Report the malaria status.
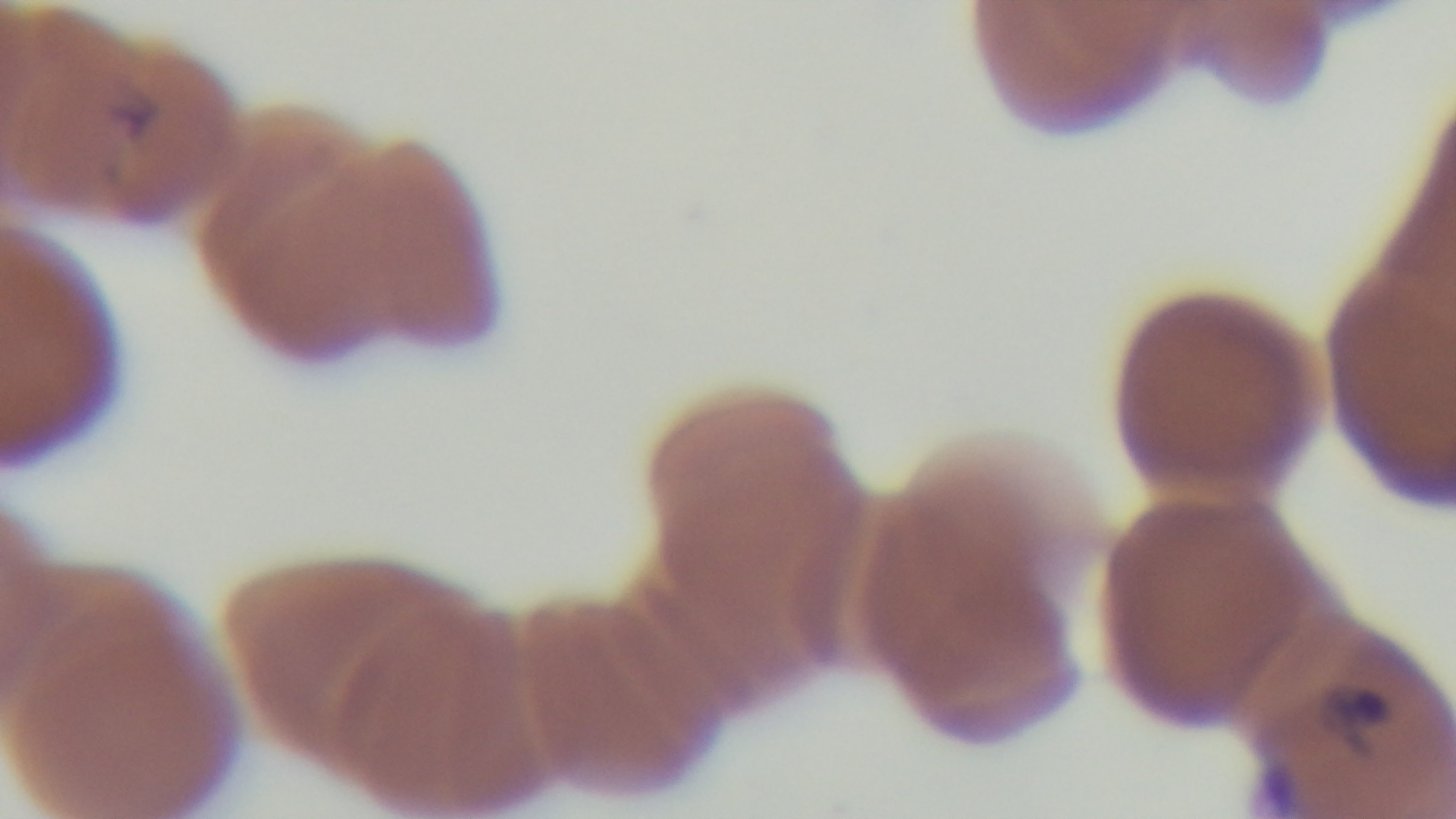

It is infected.

Summary:
  - Field of view: one from the slide
  - Capture: mounted 4K digital camera
  - Objective: 100x oil immersion
  - Preparation: thin
  - Stain: Giemsa
  - Modality: light microscopy